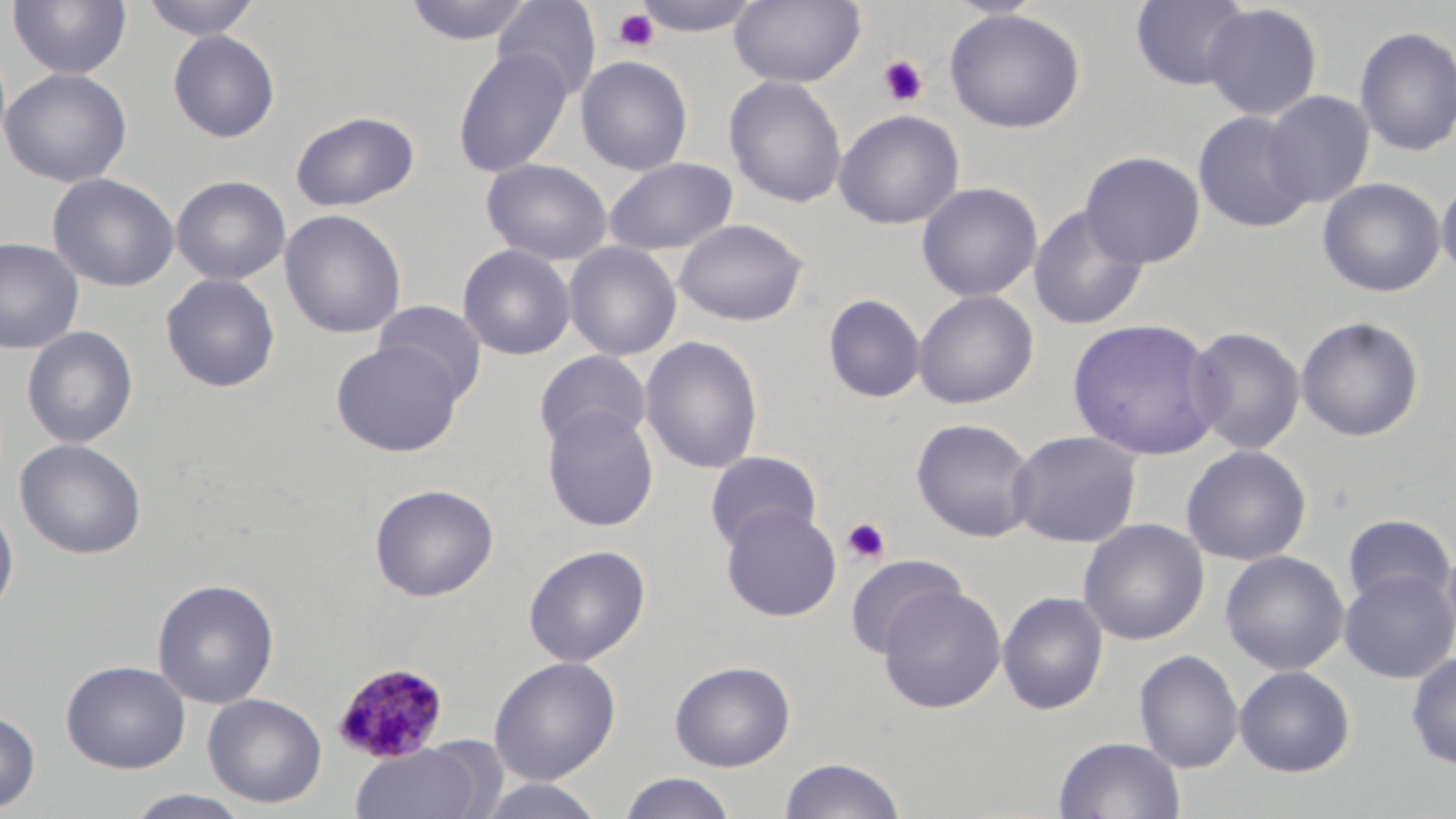
Plasmodium malariae-infected red blood cell locations = approximate bounding boxes as (x1, y1, x2, y2) in pixels: (331, 660, 451, 763)
slide-level diagnosis = Plasmodium malariae
uninfected red blood cell locations = approximate bounding boxes as (x1, y1, x2, y2) in pixels: (7, 0, 132, 80), (140, 0, 261, 41), (403, 0, 534, 46), (492, 0, 601, 101), (632, 0, 765, 37), (729, 0, 865, 87), (945, 0, 1050, 19), (1130, 0, 1253, 90), (1202, 3, 1323, 120), (944, 8, 1086, 133), (1353, 25, 1456, 157), (167, 29, 280, 143), (453, 48, 574, 178), (575, 55, 694, 176), (0, 67, 132, 188), (723, 75, 848, 208), (1261, 90, 1375, 209), (834, 109, 965, 230), (1193, 110, 1314, 233), (290, 111, 421, 211), (1080, 151, 1205, 268), (603, 157, 738, 256), (480, 158, 613, 265), (47, 173, 180, 292), (171, 175, 291, 285), (1436, 175, 1456, 282), (1317, 177, 1446, 298), (916, 182, 1043, 302), (1028, 204, 1149, 331), (279, 209, 406, 340), (673, 218, 809, 326), (0, 237, 84, 354), (563, 241, 682, 361), (458, 243, 576, 360), (160, 273, 281, 393), (913, 290, 1039, 409), (822, 293, 926, 404), (373, 300, 488, 404), (1295, 316, 1425, 442), (1067, 318, 1224, 461), (22, 326, 138, 449), (1185, 326, 1305, 455), (640, 335, 764, 474), (331, 342, 463, 456), (533, 350, 652, 454), (541, 407, 660, 532), (911, 417, 1038, 542), (1007, 429, 1143, 547), (15, 438, 147, 560), (1181, 444, 1312, 566), (705, 451, 822, 552), (369, 483, 499, 601), (0, 500, 19, 619), (720, 505, 842, 622), (1342, 513, 1454, 610), (1077, 518, 1209, 646), (523, 544, 651, 667), (1440, 544, 1456, 656), (1220, 550, 1349, 675), (844, 554, 966, 660), (1338, 568, 1456, 683), (152, 578, 279, 709), (877, 585, 1006, 713), (997, 591, 1108, 715), (1134, 649, 1243, 773), (1406, 651, 1456, 769), (488, 655, 621, 785), (61, 659, 190, 773), (669, 659, 796, 771), (1234, 665, 1355, 777), (203, 693, 327, 808), (0, 710, 40, 813), (1053, 736, 1186, 819), (349, 741, 496, 819), (779, 757, 906, 819), (617, 772, 738, 819), (481, 776, 607, 819), (123, 789, 255, 818)
modality = light microscopy
stain = May-Grünwald-Giemsa
platelet locations = approximate bounding boxes as (x1, y1, x2, y2) in pixels: (613, 7, 660, 52), (877, 55, 928, 107), (842, 517, 890, 564)
image size = 1456×819 pixels
field of view = single
magnification = 1000x
preparation = thin blood film